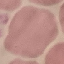
Malaria status: uninfected. Thin blood film. Cell patch, automatically extracted from a larger field of view and resized to 64 × 64 pixels. Giemsa stain. Acquired by smartphone through the microscope eyepiece.